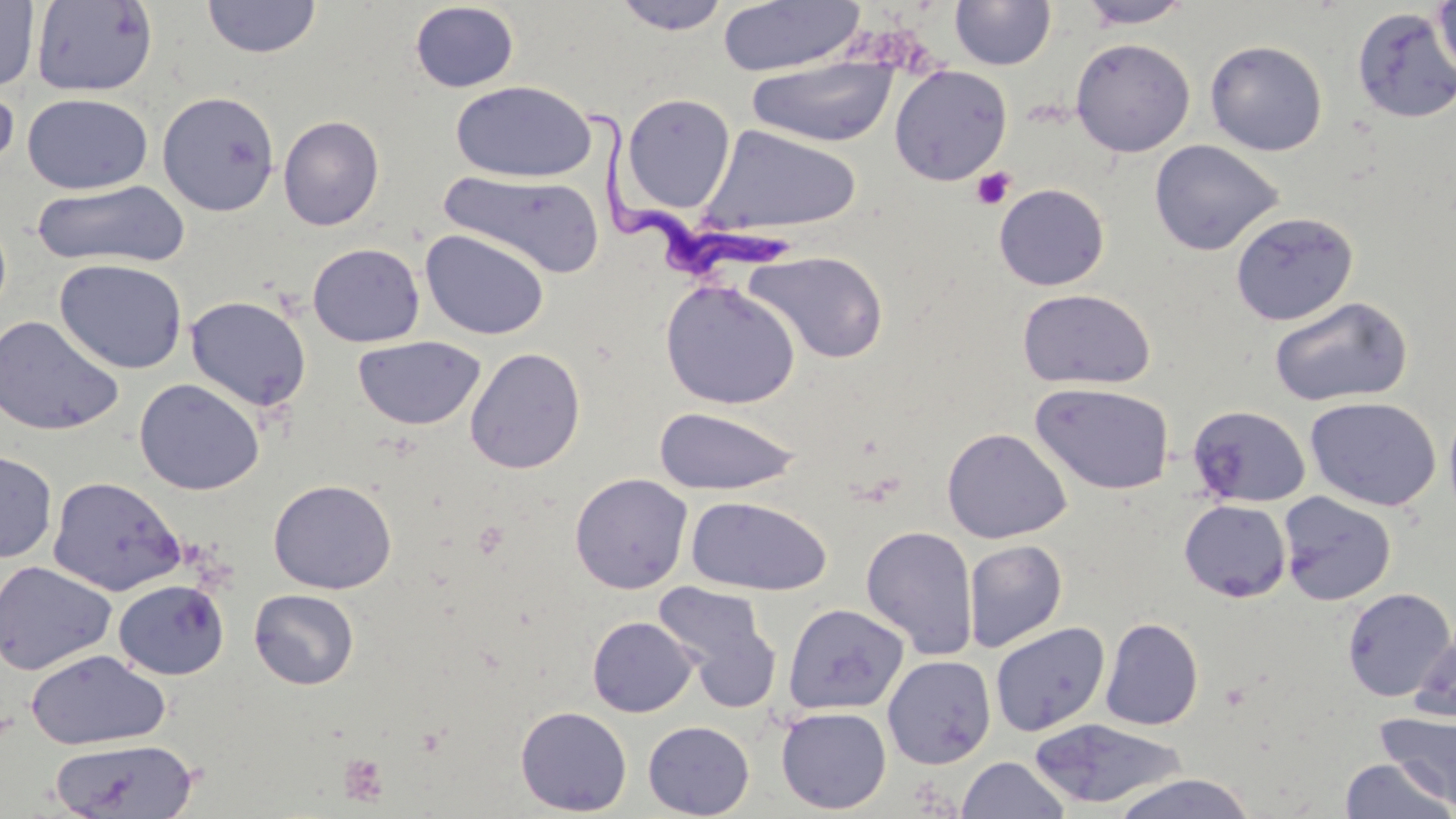
Approximate bounding boxes as named x1/y1/x2/y2 corners in pixels. Uninfected red blood cell locations: (x1=201, y1=0, x2=322, y2=59), (x1=611, y1=0, x2=732, y2=35), (x1=717, y1=0, x2=865, y2=77), (x1=1075, y1=0, x2=1195, y2=29), (x1=0, y1=1, x2=39, y2=91), (x1=31, y1=1, x2=159, y2=97), (x1=949, y1=1, x2=1056, y2=70), (x1=1433, y1=1, x2=1456, y2=82), (x1=409, y1=2, x2=520, y2=93), (x1=1352, y1=7, x2=1456, y2=123), (x1=1070, y1=37, x2=1196, y2=157), (x1=1205, y1=40, x2=1328, y2=156), (x1=746, y1=57, x2=899, y2=146), (x1=889, y1=65, x2=1012, y2=185), (x1=450, y1=80, x2=597, y2=183), (x1=0, y1=82, x2=20, y2=176), (x1=157, y1=91, x2=281, y2=216), (x1=22, y1=92, x2=154, y2=195), (x1=622, y1=93, x2=736, y2=213), (x1=278, y1=115, x2=384, y2=231), (x1=699, y1=125, x2=862, y2=235), (x1=1149, y1=139, x2=1284, y2=256), (x1=438, y1=170, x2=606, y2=278), (x1=32, y1=179, x2=190, y2=269), (x1=993, y1=183, x2=1110, y2=291), (x1=1230, y1=211, x2=1358, y2=326), (x1=421, y1=229, x2=550, y2=341), (x1=307, y1=242, x2=426, y2=347), (x1=744, y1=250, x2=888, y2=364), (x1=54, y1=258, x2=188, y2=374), (x1=660, y1=279, x2=801, y2=410), (x1=1017, y1=287, x2=1157, y2=390), (x1=185, y1=295, x2=312, y2=412), (x1=1268, y1=296, x2=1413, y2=407), (x1=0, y1=315, x2=124, y2=436), (x1=352, y1=335, x2=486, y2=430), (x1=465, y1=347, x2=586, y2=474), (x1=134, y1=378, x2=266, y2=496), (x1=1030, y1=382, x2=1175, y2=495), (x1=1305, y1=396, x2=1442, y2=512), (x1=1443, y1=399, x2=1456, y2=526), (x1=1188, y1=404, x2=1311, y2=508), (x1=652, y1=406, x2=802, y2=496), (x1=941, y1=427, x2=1071, y2=543), (x1=0, y1=449, x2=58, y2=563), (x1=570, y1=473, x2=693, y2=594), (x1=47, y1=476, x2=186, y2=596), (x1=268, y1=479, x2=397, y2=594), (x1=1278, y1=491, x2=1397, y2=606), (x1=686, y1=495, x2=832, y2=596), (x1=1178, y1=500, x2=1291, y2=602), (x1=860, y1=525, x2=979, y2=660), (x1=963, y1=539, x2=1068, y2=652), (x1=0, y1=560, x2=117, y2=676), (x1=112, y1=579, x2=230, y2=680), (x1=652, y1=581, x2=781, y2=707), (x1=1341, y1=587, x2=1456, y2=702), (x1=249, y1=588, x2=360, y2=690), (x1=783, y1=602, x2=909, y2=715), (x1=587, y1=616, x2=698, y2=718), (x1=1100, y1=617, x2=1204, y2=730), (x1=990, y1=621, x2=1110, y2=737), (x1=1409, y1=629, x2=1456, y2=724), (x1=25, y1=649, x2=170, y2=750), (x1=882, y1=655, x2=996, y2=769), (x1=515, y1=706, x2=632, y2=816), (x1=775, y1=706, x2=892, y2=815), (x1=1376, y1=710, x2=1456, y2=809), (x1=641, y1=716, x2=893, y2=814), (x1=1028, y1=718, x2=1187, y2=809), (x1=643, y1=720, x2=755, y2=818), (x1=48, y1=737, x2=200, y2=819), (x1=957, y1=756, x2=1070, y2=818), (x1=1339, y1=757, x2=1454, y2=818), (x1=1109, y1=771, x2=1259, y2=819). Platelet locations: (x1=971, y1=167, x2=1015, y2=210), (x1=338, y1=753, x2=390, y2=807). Trypanosoma brucei locations: (x1=589, y1=108, x2=798, y2=282). Slide-level diagnosis: Trypanosoma brucei. May-Grünwald-Giemsa stain. 1000x magnification. One field of a larger specimen. Image is 1456×819 pixels. Thin blood smear. Optical microscopy.